Give the position of every Plasmodium parasite visible.
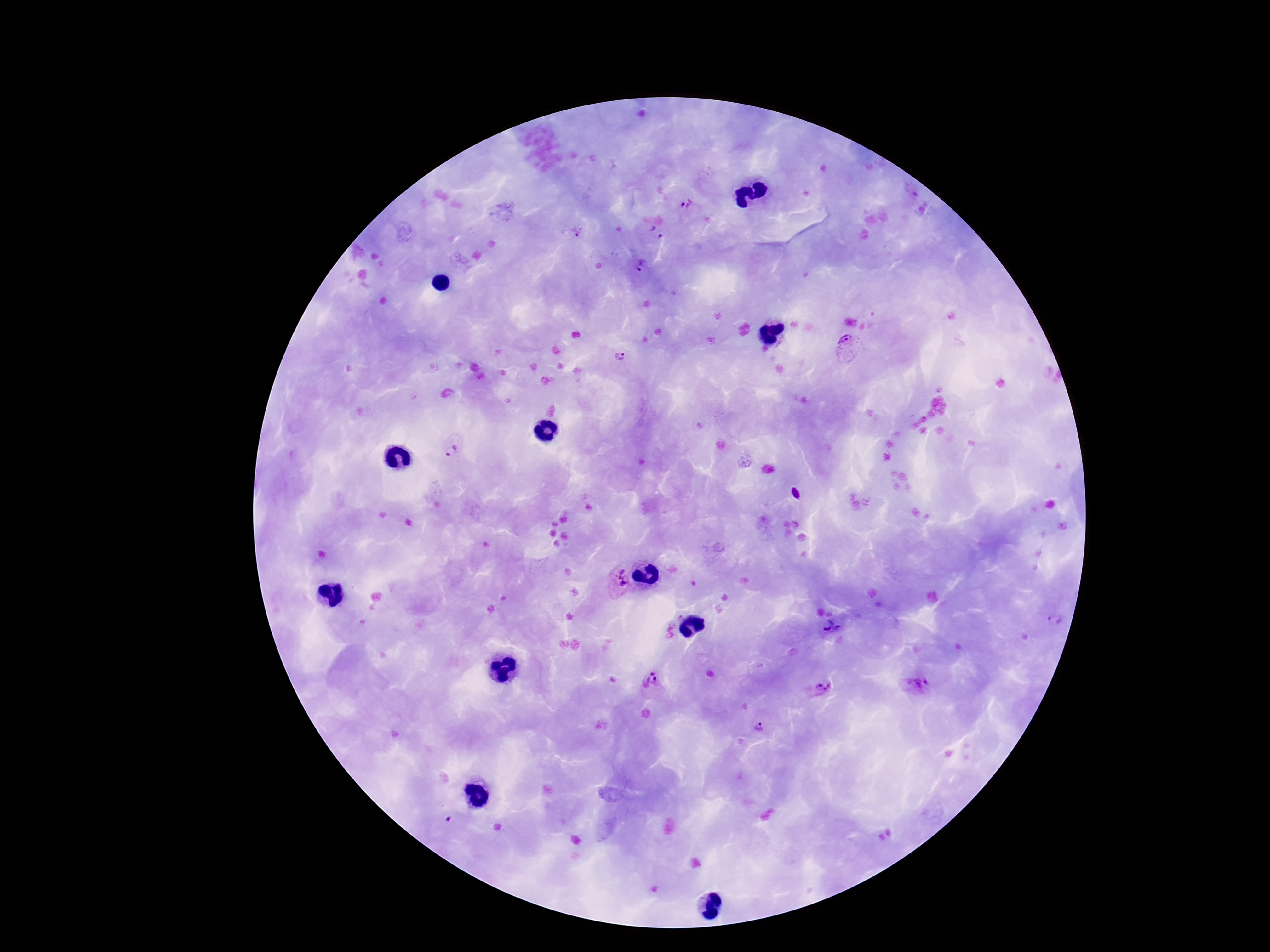
Approximate object centers, in pixels from the top-left corner.
Plasmodium parasites: (x=688, y=206), (x=577, y=233), (x=657, y=233), (x=641, y=264), (x=846, y=344), (x=620, y=357), (x=453, y=447), (x=617, y=585), (x=1055, y=621), (x=832, y=628), (x=668, y=632), (x=651, y=679), (x=916, y=685), (x=821, y=689), (x=760, y=727).

{
  "stain": "Giemsa",
  "magnification": "100x",
  "image_size": "1270×952 pixels",
  "field_of_view": "one from this slide",
  "preparation": "thick blood smear",
  "capture": "smartphone camera through the microscope eyepiece",
  "patient_malaria_status": "positive"
}